Assess this cell for malaria.
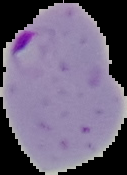

It is parasitized.

From a thin blood film. The area outside the segmented cell region is set to black. Image is 127×175 pixels.